Locate every malaria parasite.
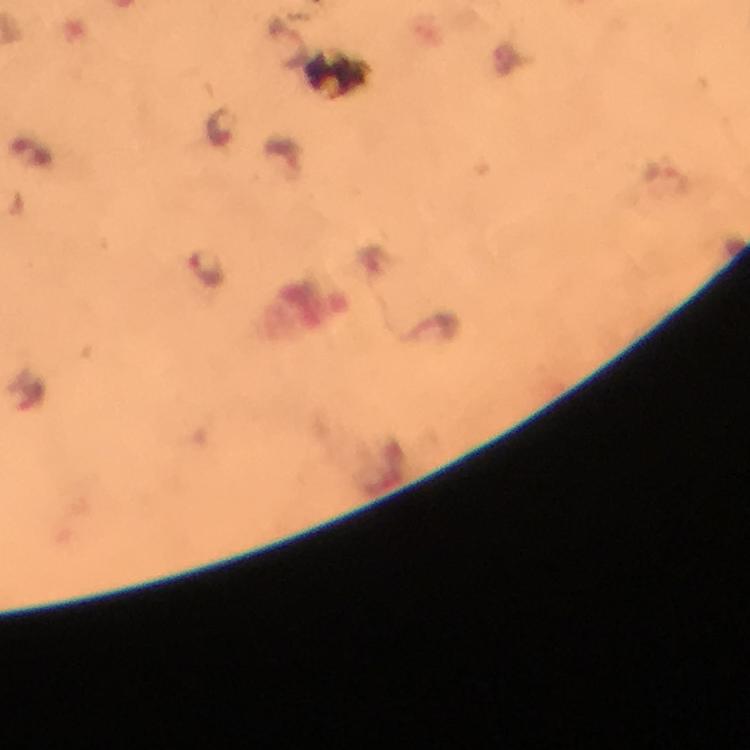
Approximate centers as {x, y} in pixels.
Malaria parasites: {221, 126}, {205, 268}.

magnification = 100x
immersion oil = used
cropped from = a single field of view
image size = 750×750 pixels
stain = Giemsa
preparation = thick smear
capture = smartphone camera through the microscope
context = from a malaria diagnostic workup